State which parasite is depicted.
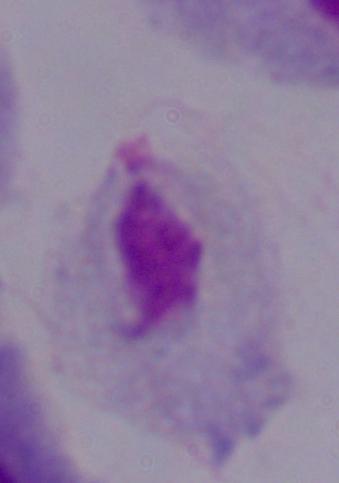
This is a trichomonad.

Micrograph. 1000x magnification.